Classify this cell by malaria status.
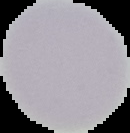

Uninfected.

preparation = thin blood smear
image type = segmented cell region on a black background
image size = 130×133 pixels